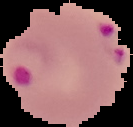

Summary:
  - Image type: cell region segmented out of the field of view; surrounding area masked to black
  - Result: malaria parasites identified
  - Image size: 133×127 pixels
  - Preparation: thin blood smear